Classify this cell by malaria status.
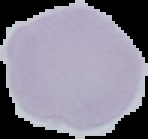
It is uninfected.

image size = 148×139 pixels
image type = segmented cell region with the area outside set to black
preparation = thin blood smear